State which parasite is depicted.
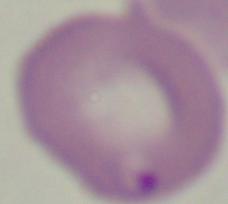
This is Babesia.

Summary:
  - Modality: photomicrograph
  - Magnification: 1000x